Comment on the morphology of the red blood cells.
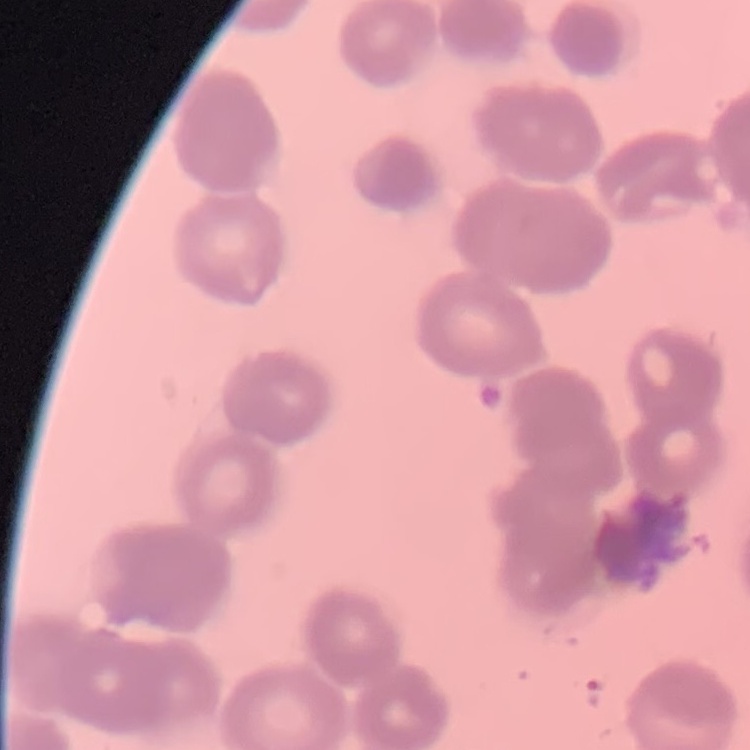
They show rouleaux formation.

One tile cut from a larger photomicrograph. Thin blood film. Field's or Giemsa stain.